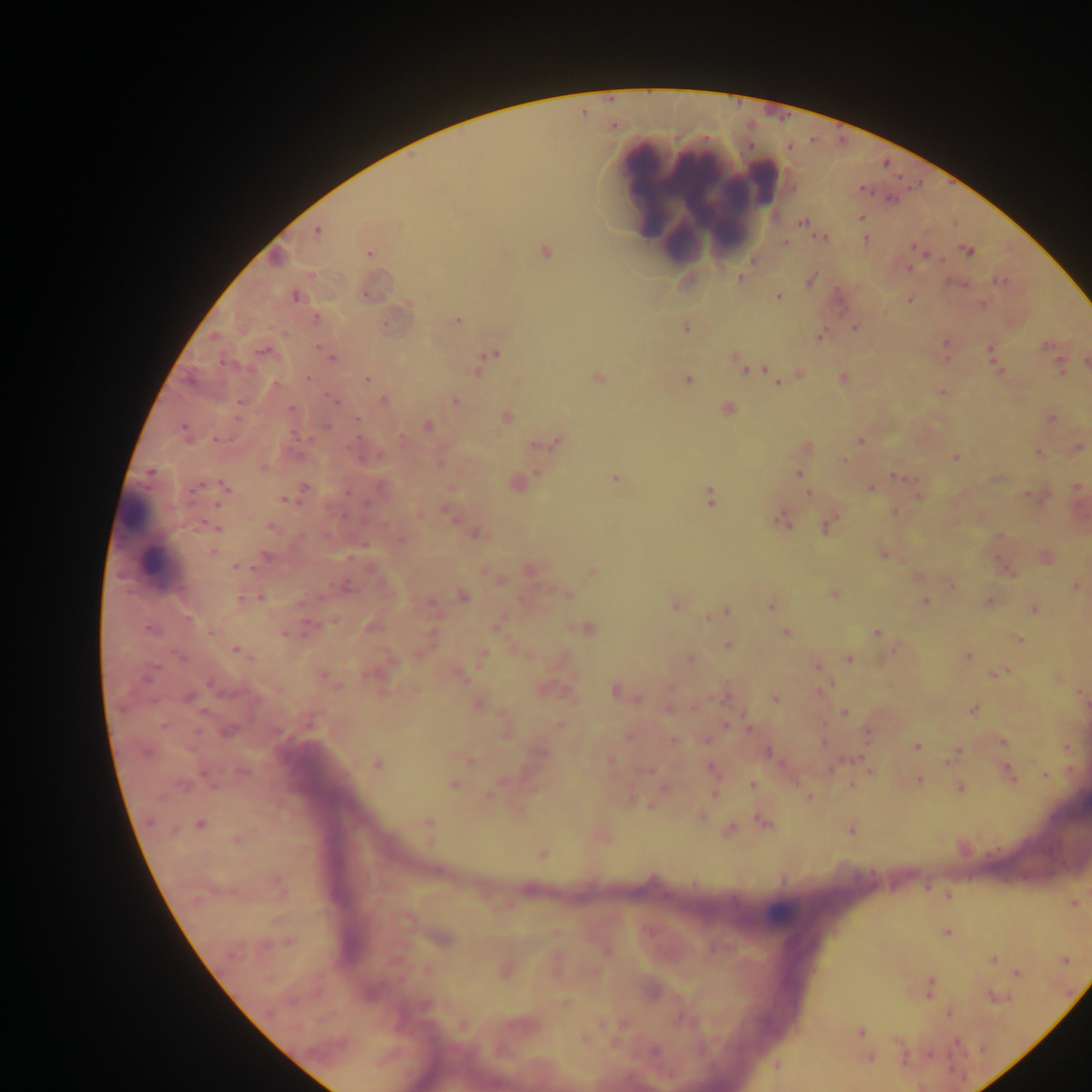
Approximate centers as [x, y] in pixels. Leukocyte locations: [698, 195], [147, 539], [783, 910]. Malaria parasite locations: [861, 217], [802, 222], [317, 232], [822, 238], [865, 239], [785, 243], [914, 248], [544, 252], [968, 252], [370, 253], [909, 267], [740, 278], [810, 279], [1000, 281], [365, 295], [295, 296], [779, 296], [909, 300], [408, 304], [315, 319], [457, 321], [854, 328], [686, 329], [821, 335], [946, 342], [1048, 346], [991, 350], [322, 351], [264, 352], [493, 353], [735, 356], [331, 357], [1086, 361], [222, 362], [740, 364], [1060, 367], [767, 369], [479, 370], [1000, 371], [799, 375], [598, 377], [308, 378], [843, 378], [368, 379], [688, 379], [516, 381], [777, 383], [942, 392], [334, 401], [384, 401], [456, 401], [239, 405], [290, 409], [728, 409], [1052, 417], [506, 418], [357, 419], [429, 425], [183, 428], [403, 437], [217, 439], [861, 440], [557, 442], [540, 444], [807, 446], [1078, 447], [1038, 452], [956, 458], [844, 460], [440, 464], [150, 472], [798, 474], [896, 476], [616, 478], [197, 487], [225, 487], [305, 487], [1077, 487], [870, 489], [809, 493], [917, 494], [710, 496], [285, 500], [218, 504], [894, 512], [447, 514], [782, 519], [271, 526], [826, 526], [217, 528], [476, 534], [401, 539], [212, 552], [883, 554], [266, 555], [236, 567], [530, 569], [590, 572], [952, 585], [346, 587], [1074, 587], [566, 593], [834, 594], [463, 596], [242, 599], [260, 599], [989, 601], [926, 602], [771, 606], [674, 607], [1034, 609], [726, 612], [706, 618], [497, 625], [372, 627], [586, 628], [149, 630], [210, 633], [284, 633], [785, 633], [876, 633], [1018, 640], [728, 645], [895, 648], [236, 650], [967, 656], [180, 657], [482, 657], [849, 659], [690, 660], [817, 667], [999, 673], [148, 676], [324, 676], [210, 685], [822, 688], [616, 691], [189, 697], [721, 698], [775, 698], [478, 705], [670, 710], [973, 710], [844, 712], [560, 725], [162, 726], [726, 726], [228, 731], [279, 731], [867, 733], [629, 736], [673, 741], [1003, 742], [823, 743], [916, 746], [145, 752], [541, 752], [768, 752], [955, 754], [468, 759], [610, 760], [377, 764], [711, 768], [648, 771], [244, 772], [1009, 773], [1044, 774], [919, 779], [453, 785], [753, 785], [851, 785], [184, 787], [960, 788], [713, 793], [487, 795], [807, 796], [650, 805], [702, 817], [150, 822], [428, 822], [764, 823], [200, 825], [729, 830], [851, 831], [237, 840], [542, 854], [276, 882], [1073, 903], [946, 933], [290, 942], [605, 949], [992, 959], [1066, 961], [1017, 974], [930, 984], [996, 997], [564, 1002], [948, 1013], [861, 1031], [957, 1043], [654, 1051], [870, 1057], [777, 1066]. Image is 1092×1092 pixels. Thick blood film. One field of view. Photographed through a microscope with a mobile-phone camera. Collected in Ghana.